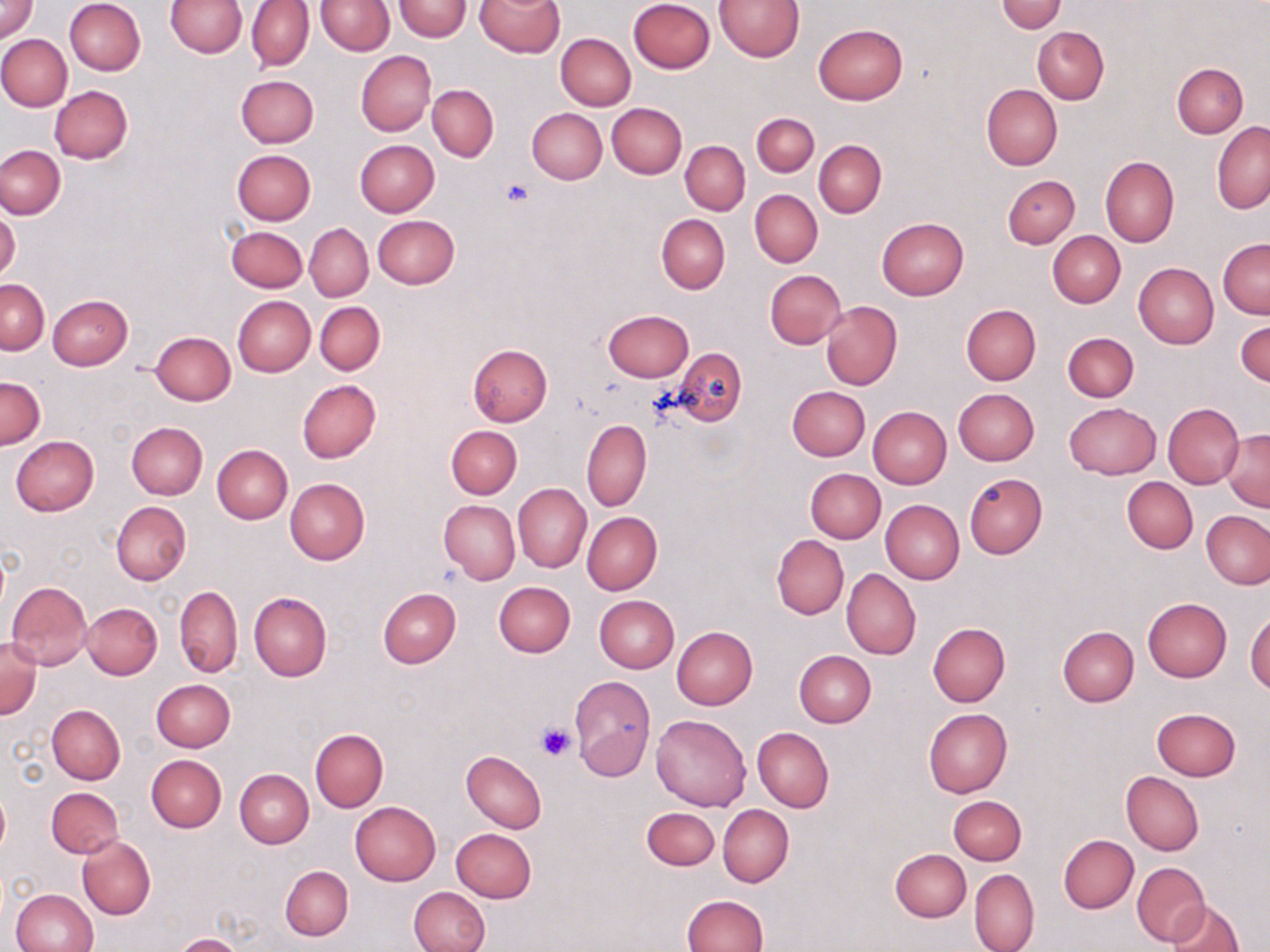
Approximate bounding boxes as (x1, y1, x2, y2) in pixels. Uninfected red blood cell locations: (1, 0, 39, 42), (64, 0, 145, 76), (165, 0, 247, 58), (476, 0, 564, 57), (629, 0, 714, 73), (714, 0, 803, 61), (246, 1, 314, 71), (318, 1, 393, 54), (394, 1, 471, 41), (997, 1, 1067, 34), (814, 24, 907, 104), (1033, 27, 1109, 104), (555, 32, 636, 110), (0, 34, 73, 111), (355, 51, 435, 136), (1172, 62, 1248, 138), (236, 74, 318, 148), (981, 83, 1062, 171), (50, 85, 132, 163), (427, 85, 499, 160), (607, 102, 687, 179), (527, 109, 606, 184), (751, 113, 818, 177), (1212, 121, 1270, 215), (363, 139, 444, 292), (355, 140, 439, 217), (814, 140, 886, 218), (681, 142, 750, 214), (0, 145, 66, 219), (232, 149, 316, 224), (1099, 156, 1179, 248), (1003, 175, 1079, 247), (750, 189, 822, 267), (0, 211, 21, 284), (656, 213, 730, 294), (373, 215, 459, 288), (876, 217, 969, 300), (305, 223, 373, 301), (311, 225, 378, 376), (225, 226, 307, 293), (1048, 230, 1125, 307), (1218, 239, 1270, 318), (1134, 263, 1218, 349), (765, 270, 846, 349), (0, 278, 49, 353), (48, 295, 133, 370), (232, 296, 314, 377), (315, 301, 385, 375), (820, 301, 902, 390), (961, 305, 1041, 385), (601, 310, 692, 381), (1235, 319, 1270, 388), (151, 331, 235, 405), (1062, 332, 1139, 402), (468, 343, 552, 427), (675, 347, 746, 426), (0, 377, 45, 449), (296, 379, 381, 464), (788, 386, 870, 461), (953, 388, 1039, 466), (1163, 402, 1244, 490), (1064, 403, 1161, 479), (867, 406, 950, 489), (581, 418, 652, 512), (126, 422, 207, 500), (446, 425, 521, 499), (1221, 430, 1270, 512), (10, 436, 98, 516), (212, 444, 292, 524), (806, 468, 885, 542), (963, 472, 1047, 560), (1123, 477, 1198, 553), (285, 478, 370, 565), (513, 483, 590, 572), (439, 499, 519, 586), (881, 499, 963, 585), (111, 501, 191, 585), (1201, 511, 1269, 589), (583, 512, 663, 594), (772, 535, 848, 619), (842, 568, 921, 660), (6, 580, 92, 669), (494, 582, 575, 658), (175, 586, 243, 677), (377, 588, 460, 668), (249, 592, 330, 682), (594, 595, 679, 672), (1143, 597, 1231, 682), (82, 602, 162, 679), (1246, 612, 1270, 693), (928, 622, 1010, 706), (672, 626, 758, 708), (1058, 626, 1139, 706), (0, 638, 41, 718), (794, 650, 876, 727), (569, 677, 656, 780), (151, 679, 235, 752), (47, 704, 125, 784), (1151, 706, 1240, 781), (923, 709, 1013, 798), (652, 714, 750, 811), (753, 727, 833, 812), (309, 729, 387, 812), (462, 750, 545, 832), (146, 754, 226, 832), (235, 768, 313, 848), (1121, 772, 1204, 856), (46, 787, 124, 858), (0, 791, 10, 857), (949, 795, 1026, 865), (350, 801, 441, 885), (718, 805, 793, 886), (642, 807, 718, 870), (451, 828, 537, 903), (1059, 835, 1138, 913), (77, 836, 156, 920), (890, 848, 971, 921), (1131, 862, 1211, 948), (280, 865, 352, 941), (968, 869, 1040, 952), (408, 886, 489, 952), (10, 888, 97, 952), (682, 894, 768, 952), (1168, 901, 1244, 952), (174, 933, 246, 952). Platelet locations: (502, 179, 535, 207), (536, 721, 577, 762). Slide-level diagnosis: negative for blood parasites. Thin blood film. May-Grünwald-Giemsa stain. Image is 1270×952 pixels. One field of a larger specimen. Light microscopy. Captured at 1000x magnification.